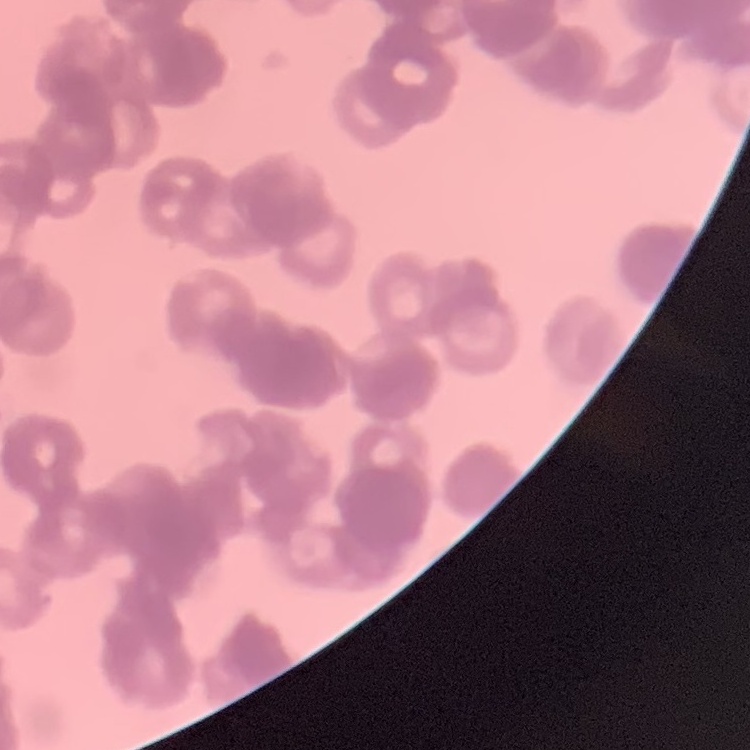
The red blood cells exhibit rouleaux formation. Field's or Giemsa stain. Thin blood smear. One tile cut from a larger photomicrograph.